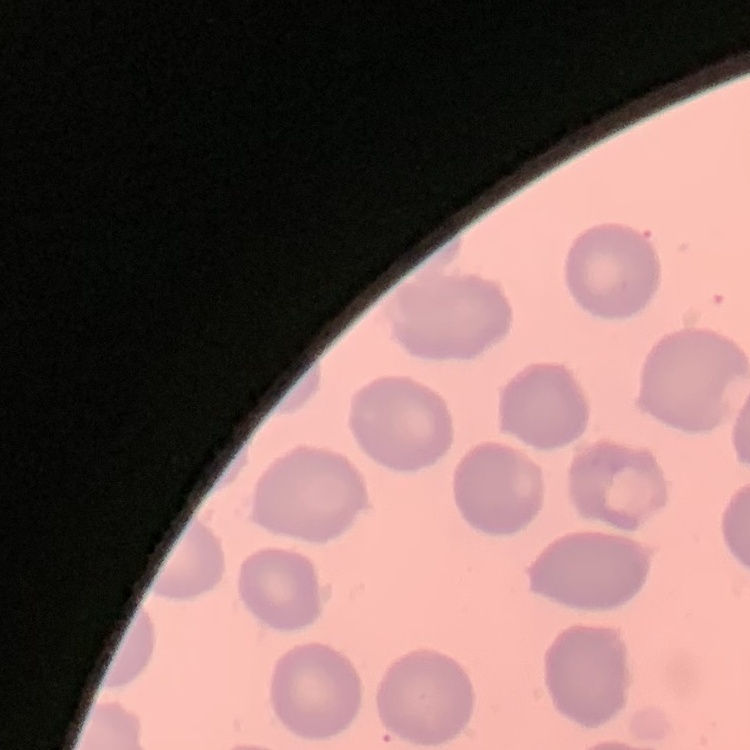 The red blood cells show no rouleaux formation. Thin blood smear. Stained with either Field's or Giemsa. One tile cut from a larger photomicrograph.